Identify the parasite.
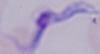
A trypanosome.

1000x magnification. Micrograph.